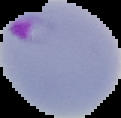

Summary:
  - Image type: segmented cell region on a black background
  - Preparation: thin blood film
  - Result: malaria parasites identified
  - Image size: 121×118 pixels